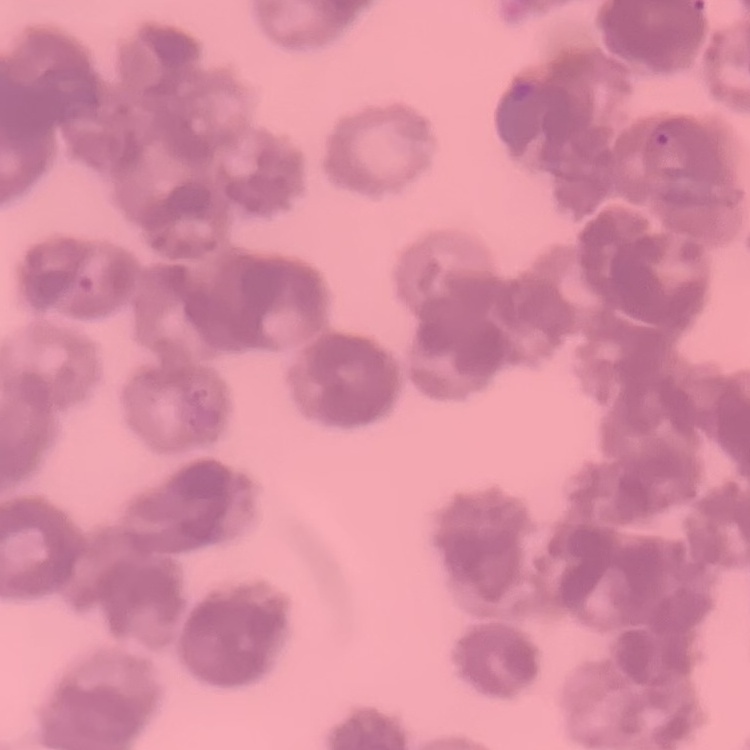

The erythrocytes exhibit rouleaux formation. Stained with either Field's or Giemsa. Thin peripheral smear. One tile cut from a larger photomicrograph.